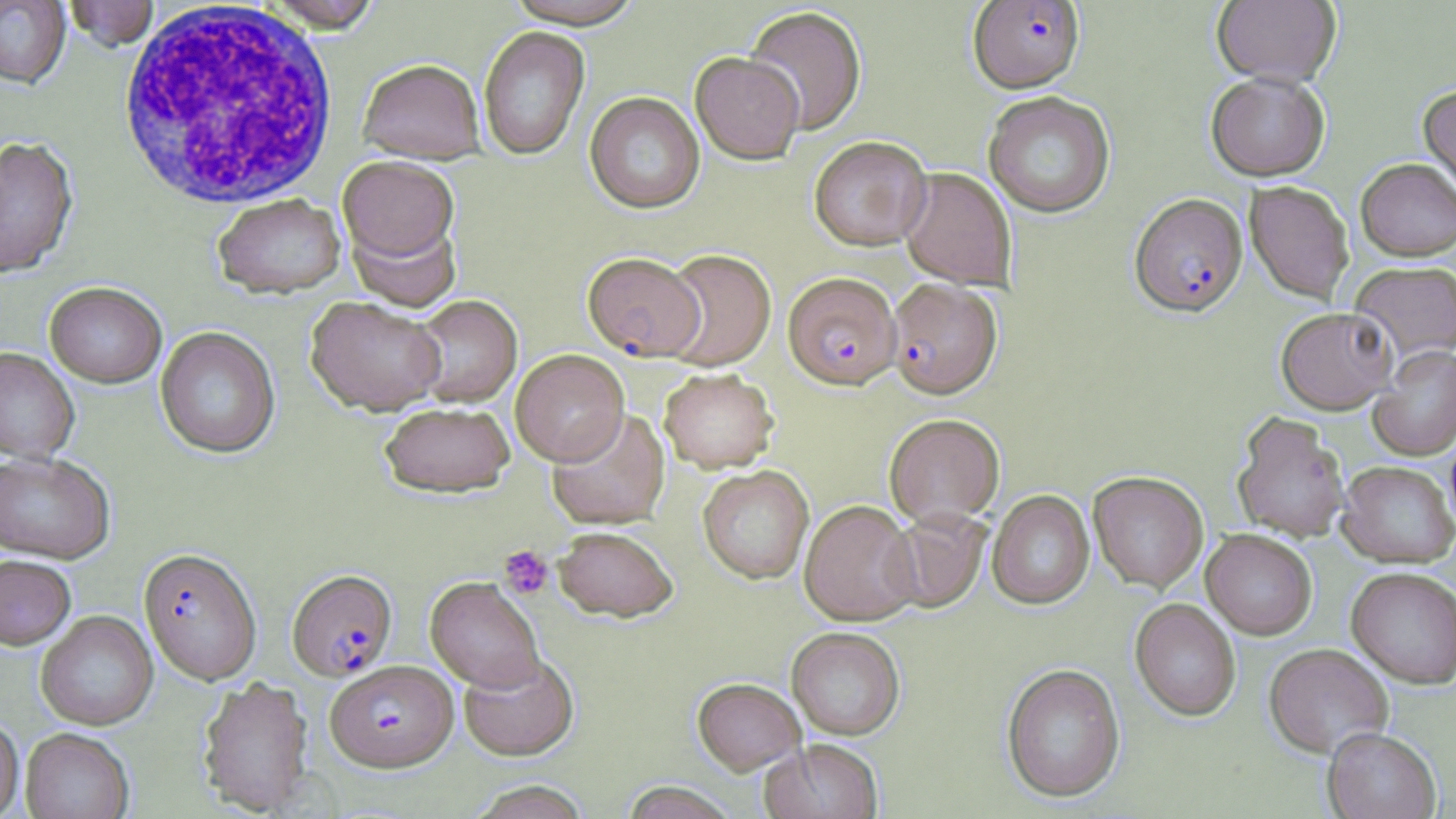

slide-level diagnosis = Plasmodium falciparum
platelet locations = approximate bounding boxes as (x1,y1)-(x2,y2) corner pairs in pixels: (499,545)-(554,599)
uninfected red blood cell locations = approximate bounding boxes as (x1,y1)-(x2,y2) corner pairs in pixels: (260,0)-(384,36), (503,0)-(647,30), (1212,0)-(1341,87), (0,1)-(71,89), (63,1)-(158,53), (744,7)-(867,136), (479,27)-(590,161), (690,52)-(805,165), (358,61)-(485,164), (1205,71)-(1330,181), (1418,84)-(1456,202), (983,91)-(1115,218), (585,92)-(705,214), (0,136)-(78,278), (808,136)-(932,251), (337,156)-(458,265), (1356,158)-(1456,261), (899,168)-(1017,290), (1245,181)-(1354,304), (212,194)-(346,299), (347,216)-(462,312), (660,249)-(776,372), (1350,262)-(1456,361), (44,281)-(167,387), (410,295)-(522,408), (305,297)-(447,415), (1276,307)-(1397,414), (155,326)-(280,459), (1367,345)-(1456,461), (0,346)-(80,462), (510,349)-(629,466), (659,368)-(779,473), (379,401)-(515,498), (546,407)-(670,530), (1232,412)-(1351,543), (884,414)-(1005,527), (1445,426)-(1456,536), (0,451)-(115,563), (1337,461)-(1455,567), (698,465)-(814,584), (1088,471)-(1208,593), (987,490)-(1094,610), (799,500)-(921,626), (886,508)-(990,613), (553,526)-(678,622), (1201,529)-(1317,640), (0,554)-(77,650), (1346,566)-(1456,688), (425,577)-(544,691), (1130,598)-(1241,721), (35,610)-(159,731), (787,627)-(905,740), (1264,644)-(1393,758), (458,652)-(579,761), (1001,663)-(1126,804), (197,676)-(315,815), (693,678)-(805,775), (0,716)-(24,819), (1322,727)-(1441,819), (21,728)-(134,819), (761,740)-(883,819), (466,780)-(594,818), (619,782)-(740,819)
white blood cell locations = approximate bounding boxes as (x1,y1)-(x2,y2) corner pairs in pixels: (116,2)-(340,210)
preparation = thin blood film
field of view = single
image size = 1456×819 pixels
Plasmodium falciparum-infected red blood cell locations = approximate bounding boxes as (x1,y1)-(x2,y2) corner pairs in pixels: (968,1)-(1084,93), (1129,193)-(1248,317), (582,252)-(706,361), (783,272)-(902,390), (887,278)-(1002,400), (139,547)-(262,685), (287,568)-(397,680), (325,659)-(458,772)
magnification = 1000x
modality = light microscopy
stain = May-Grünwald-Giemsa